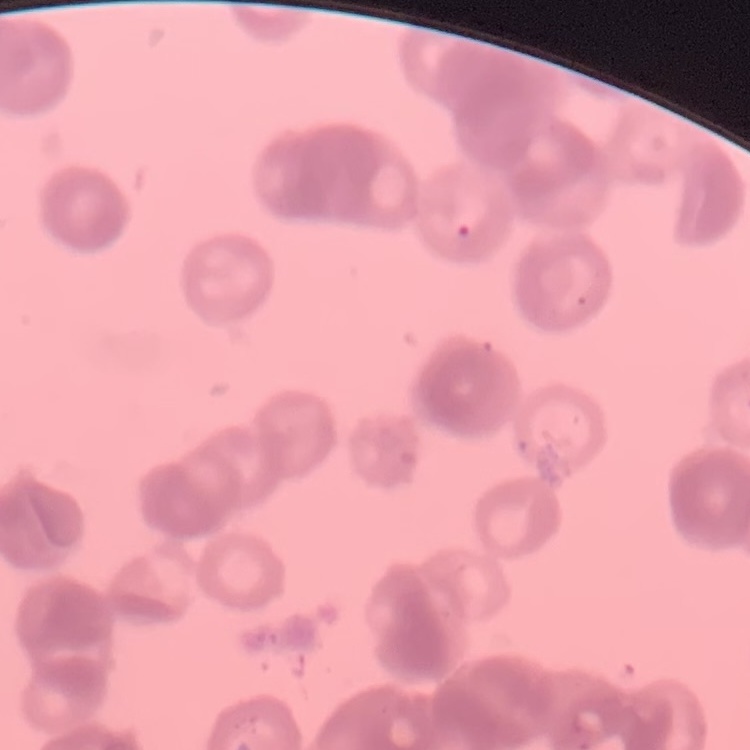

red blood cell morphology = rouleaux formation
image type = one tile cut from a larger photomicrograph
stain = Field's or Giemsa
preparation = thin blood film